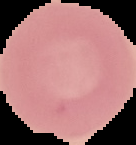
Summary:
  - Image size: 136×145 pixels
  - Malaria status: uninfected
  - Image type: segmented cell region on a black background
  - Preparation: thin blood smear